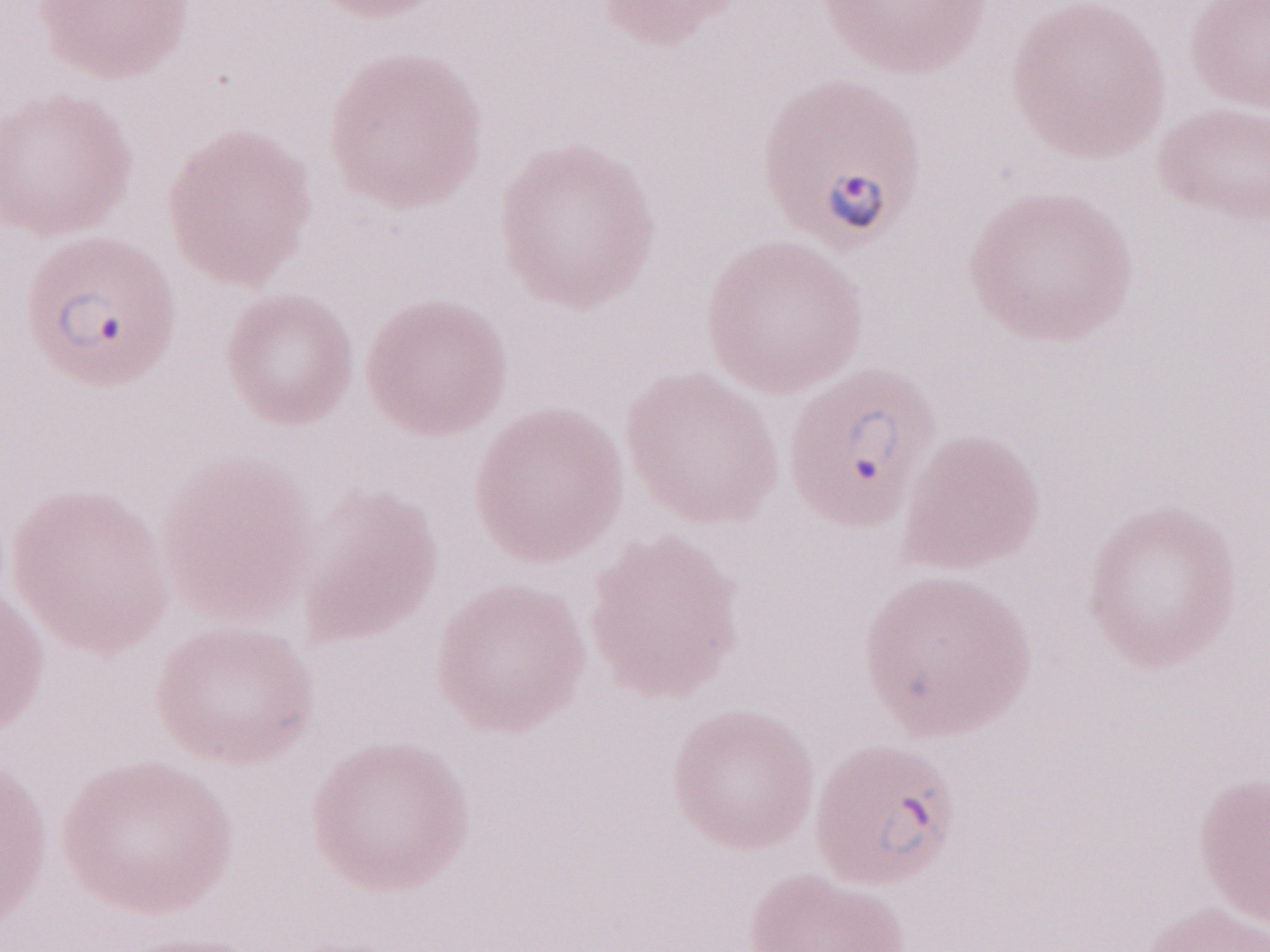
Olympus BX43 microscope, Olympus DP73 camera. Image is 1270×952 pixels. Patient diagnosis: malaria infection. May-Grünwald-Giemsa (MGG) stain. One field of this slide. Thin blood film. 1,000x magnification.